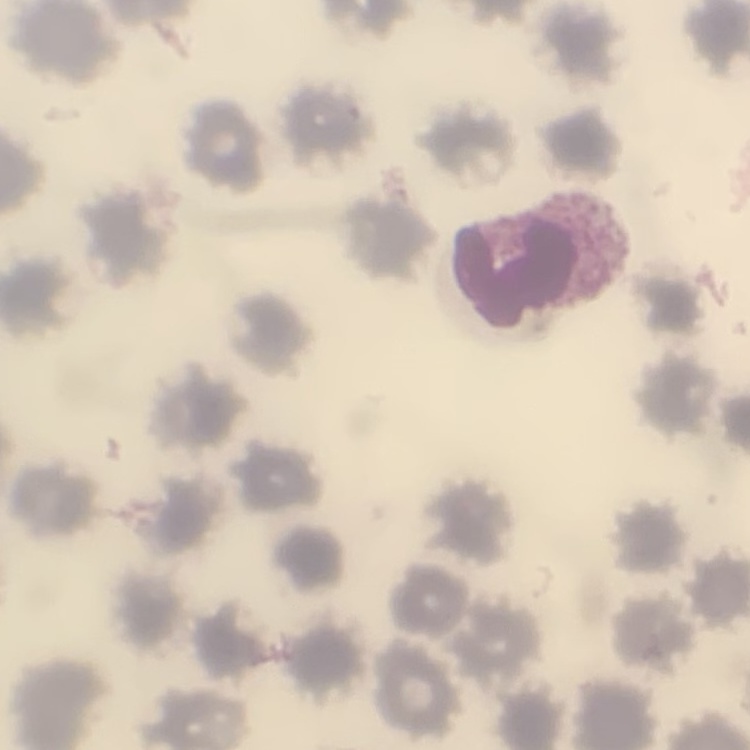 The erythrocytes exhibit no rouleaux formation. Square crop of a larger photomicrograph. Thin blood smear. Stained with either Field's or Giemsa.